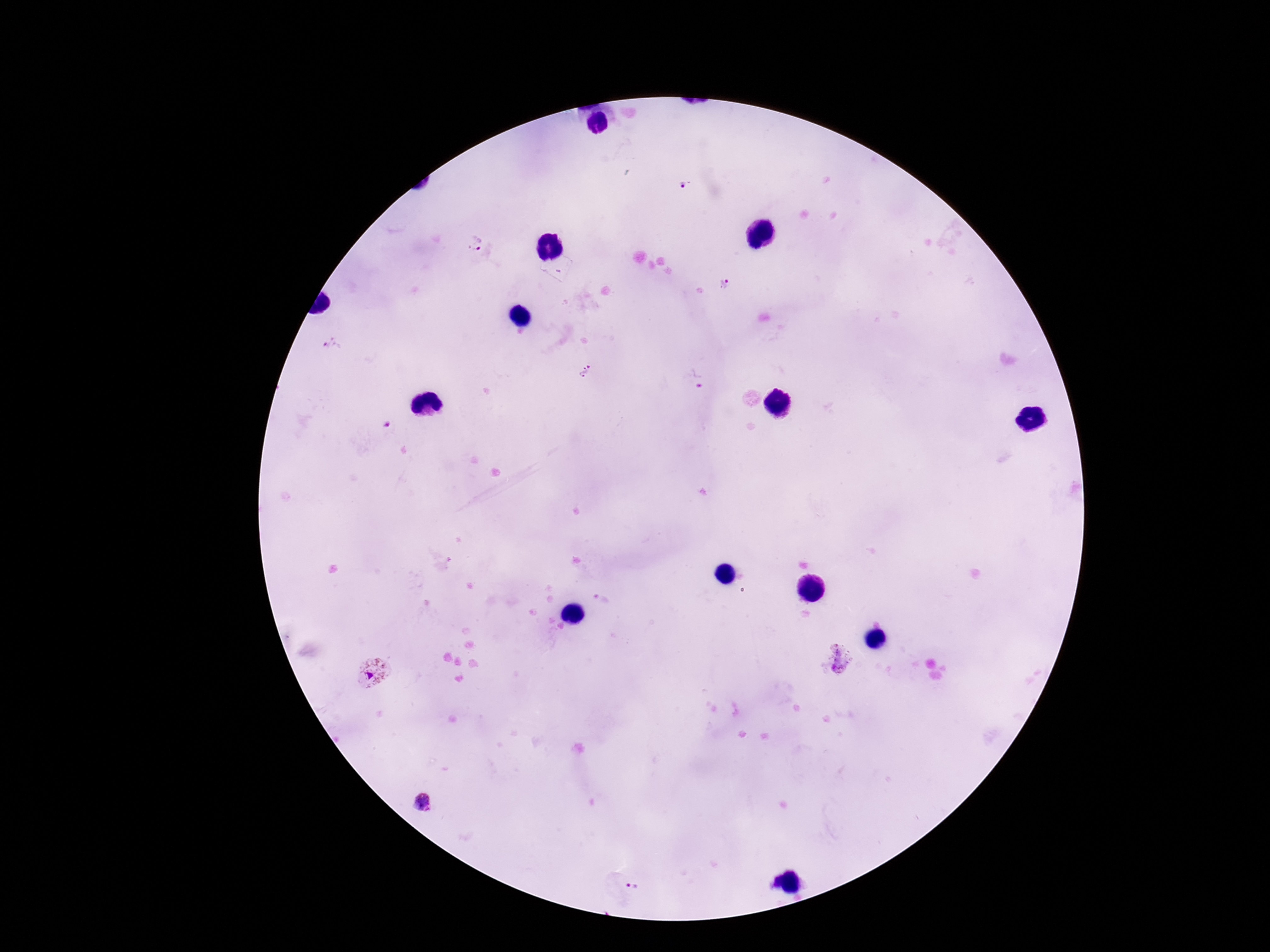 Approximate centers as {x, y} in pixels. Plasmodium parasite locations: {684, 184}, {477, 245}, {725, 282}, {331, 345}, {587, 371}, {696, 378}, {601, 599}, {838, 659}, {377, 674}, {423, 805}, {629, 887}. Smartphone photograph taken through the microscope eyepiece. 100x magnification. Giemsa-stained preparation. Image is 1270×952 pixels. Patient malaria status: infected. Single field of view. Thick blood smear.